Comment on the morphology of the erythrocytes.
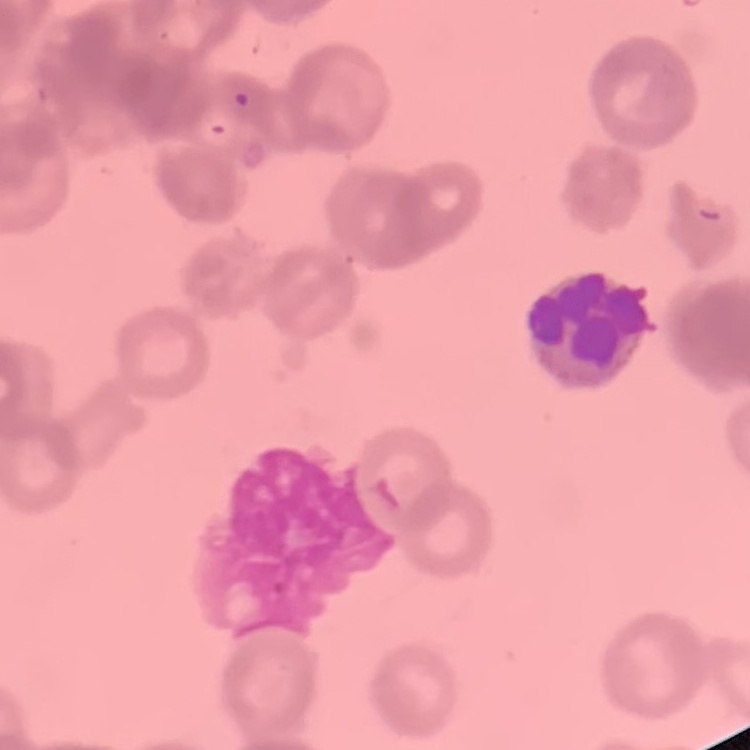

Rouleaux formation.

image_type: one tile cut from a larger photomicrograph
preparation: thin peripheral smear
stain: Field's or Giemsa